Classify this cell by malaria status.
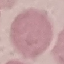
It is uninfected.

Summary:
  - Capture: smartphone camera at the microscope eyepiece
  - Preparation: thin smear
  - Stain: Giemsa
  - Image type: cell patch, automatically extracted from a larger field of view and resized to 64 × 64 pixels